Name the parasite shown.
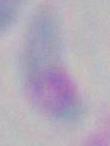
Toxoplasma gondii.

Captured at 1000x magnification. Micrograph.